Assess this cell for malaria.
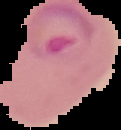
Parasitized.

Image is 121×130 pixels. Cell region segmented out of the field of view; the surrounding area is masked to black. From a thin blood film.